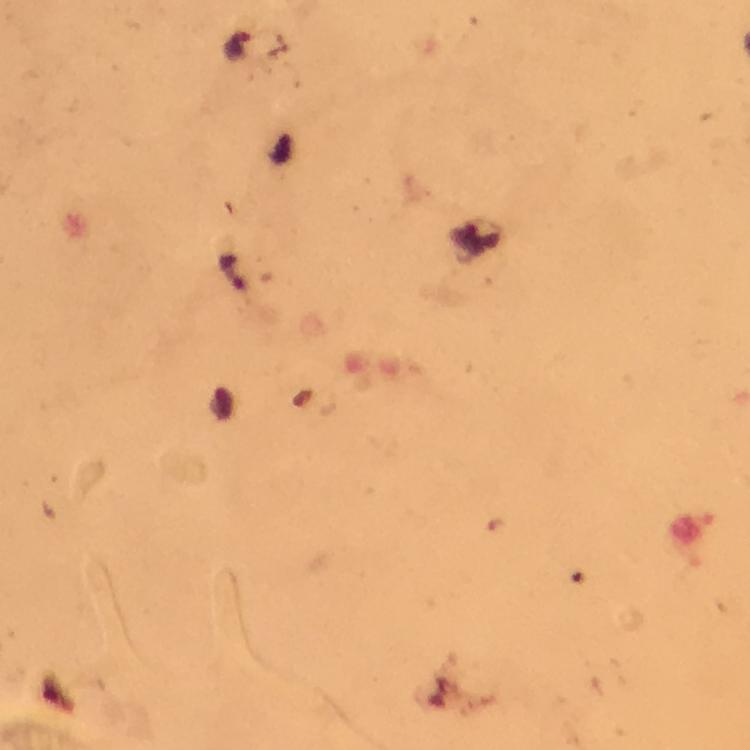
malaria parasite locations = approximate object centers, in pixels from the top-left corner: (x=237, y=46)
capture = smartphone camera through the microscope
immersion oil = used
preparation = thick blood film
context = from a malaria diagnostic workup
image size = 750×750 pixels
magnification = 100x
stain = Giemsa
cropped from = one field of view